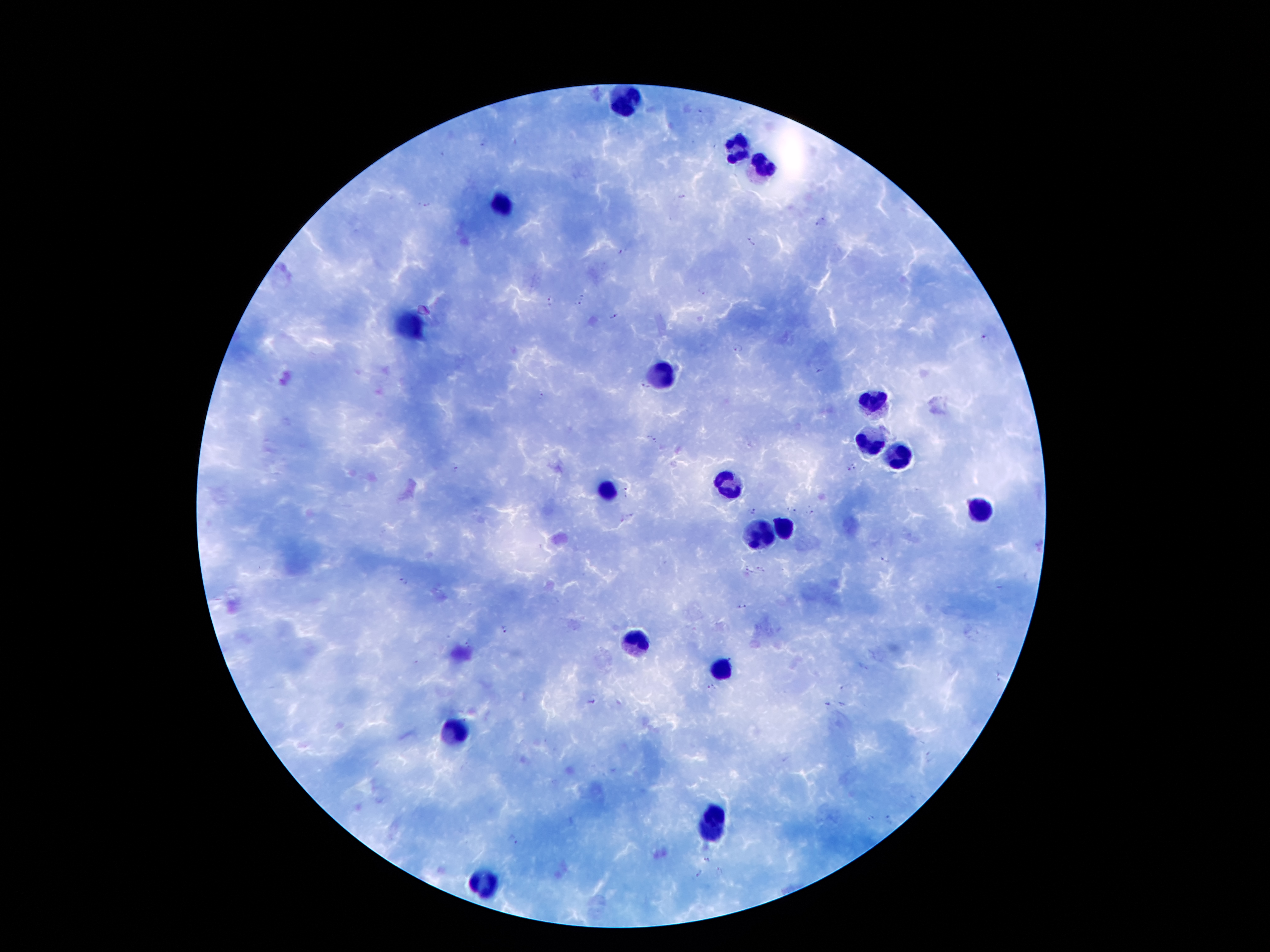
coordinate format = approximate object centers, in pixels from the top-left corner
leukocyte locations = (x=623, y=102), (x=740, y=150), (x=764, y=165), (x=503, y=203), (x=410, y=324), (x=657, y=372), (x=872, y=402), (x=870, y=441), (x=901, y=458), (x=729, y=486), (x=606, y=491), (x=981, y=508), (x=786, y=527), (x=765, y=532), (x=637, y=638), (x=721, y=671), (x=457, y=731), (x=714, y=811), (x=711, y=834), (x=481, y=887)
malaria parasite locations = (x=698, y=110), (x=485, y=143), (x=680, y=198), (x=425, y=204), (x=820, y=222), (x=750, y=242), (x=622, y=251), (x=701, y=292), (x=580, y=298), (x=552, y=300), (x=614, y=316), (x=984, y=339), (x=737, y=349), (x=819, y=370), (x=643, y=389), (x=542, y=398), (x=651, y=442), (x=852, y=468), (x=454, y=469), (x=626, y=493), (x=810, y=509), (x=753, y=510), (x=795, y=511), (x=630, y=515), (x=885, y=560), (x=760, y=569), (x=746, y=570), (x=402, y=580), (x=741, y=607), (x=504, y=630), (x=468, y=640), (x=999, y=675), (x=711, y=685), (x=845, y=687), (x=590, y=701), (x=827, y=703), (x=843, y=705), (x=929, y=758), (x=872, y=818), (x=889, y=819), (x=514, y=840), (x=709, y=860), (x=697, y=873)
field of view = one from this slide
preparation = thick blood film
patient malaria status = infected with Plasmodium falciparum
capture = smartphone camera through the microscope eyepiece
image size = 1270×952 pixels
stain = Giemsa
magnification = 100x